Assess the morphology of the red blood cells.
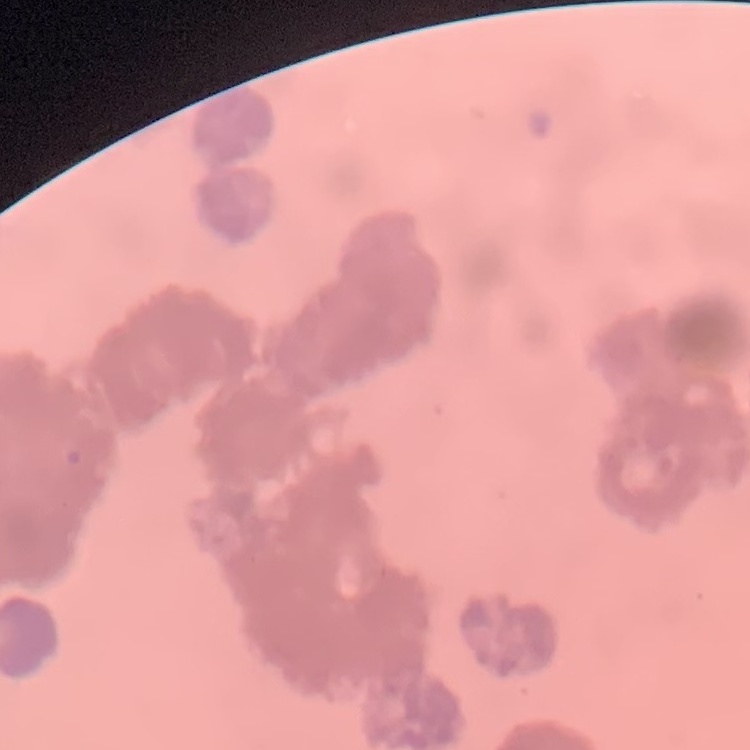

Rouleaux formation.

Field's or Giemsa stain. Square crop of a larger photomicrograph. Thin blood smear.